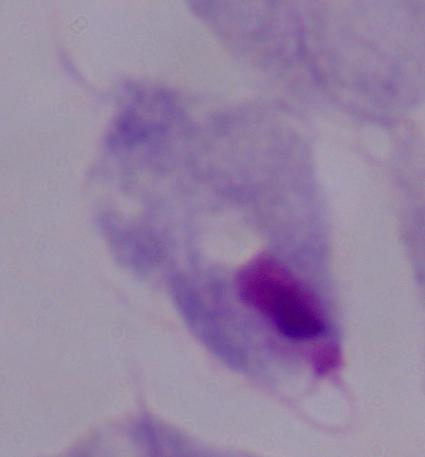
Summary:
  - Magnification: 1000x
  - Modality: photomicrograph
  - Identification: trichomonad